Assess the morphology of the red blood cells.
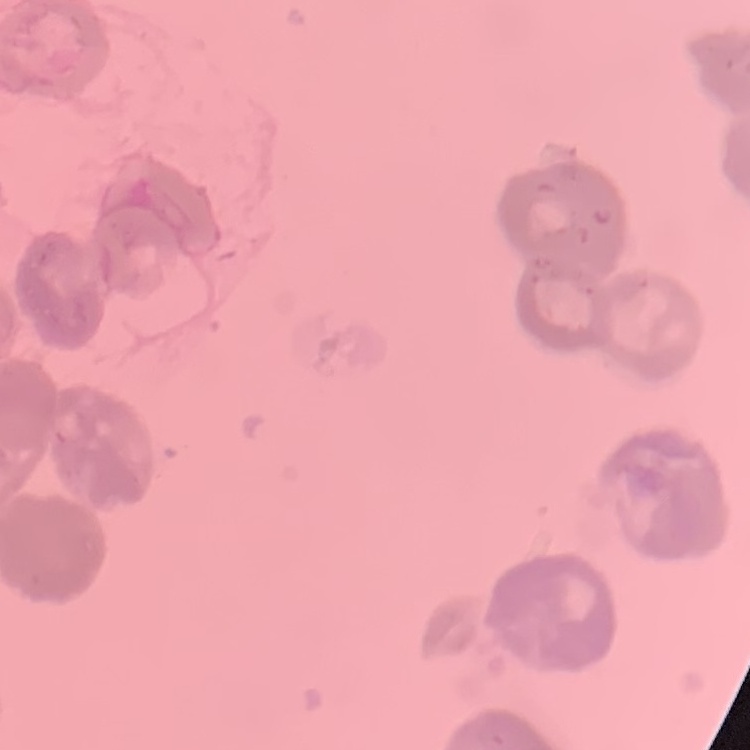
Rouleaux formation.

stain = Field's or Giemsa
image type = square crop of a larger photomicrograph
preparation = thin blood smear